Point out each leukocyte.
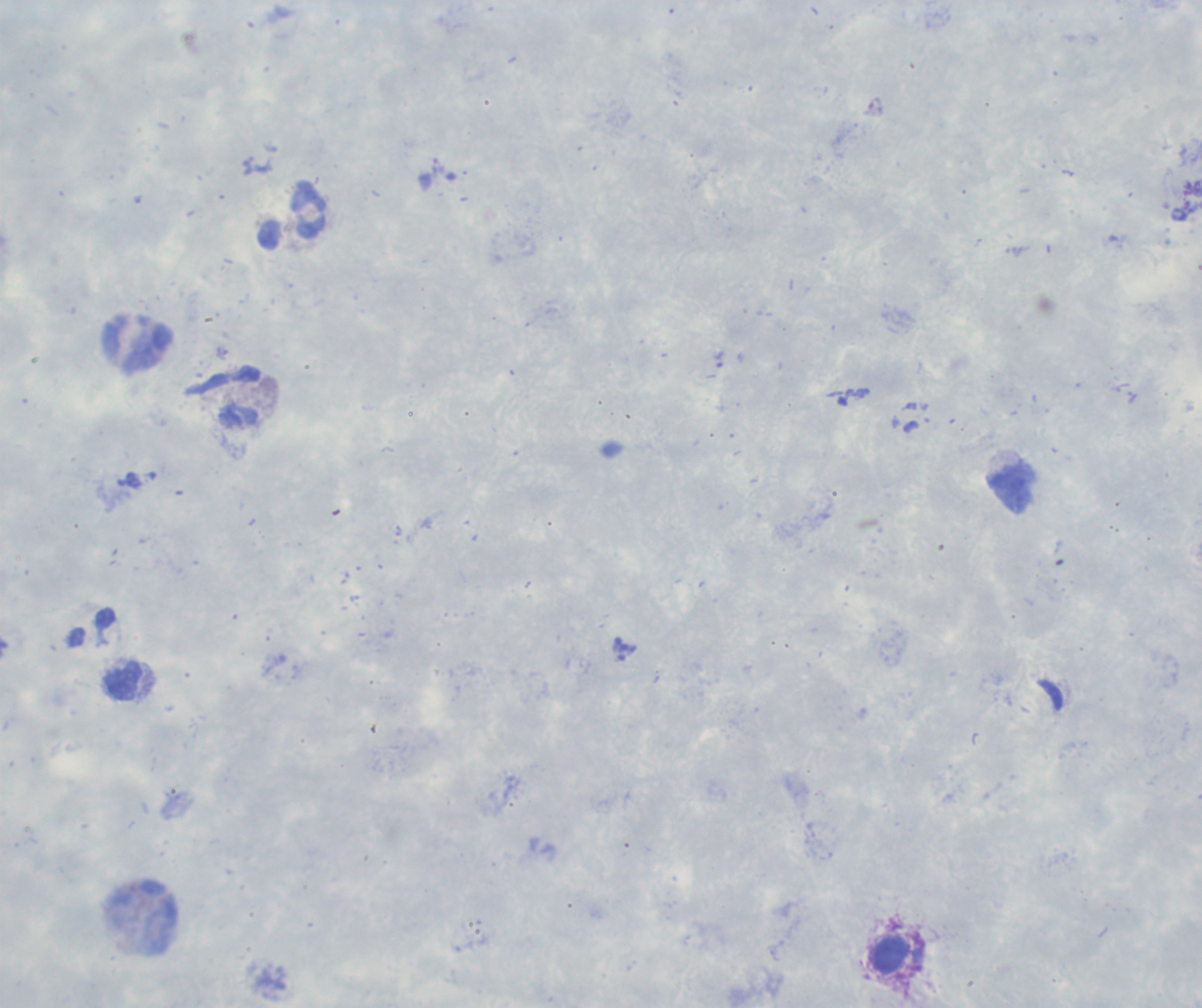

Approximate object centers, in pixels from the top-left corner.
Leukocytes: (x=292, y=215), (x=138, y=343), (x=239, y=396), (x=1011, y=488), (x=123, y=681), (x=890, y=955).

Summary:
  - Result: no malaria parasites seen
  - Image size: 1202×1008 pixels
  - Stain: Romanowsky
  - Coloration quality: good
  - Context: previously used in an actual diagnosis
  - Background quality: poor
  - Magnification: 100x
  - Field of view: single
  - Preparation: thick blood smear